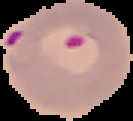

malaria_status: parasitized
image_size: 133×121 pixels
preparation: thin blood smear
image_type: segmented cell region on a black background